Classify this cell by malaria status.
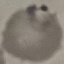
Parasitized.

preparation = thin blood film
capture = smartphone camera at the microscope eyepiece
stain = Giemsa
image type = cell patch, automatically extracted from a larger field of view and resized to 64 × 64 pixels